Report the malaria status of this cell.
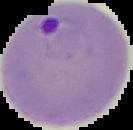

It is parasitized.

Summary:
  - Image size: 133×130 pixels
  - Preparation: thin blood smear
  - Image type: cell region segmented out of the field of view; surrounding area masked to black